Name the blood parasite species.
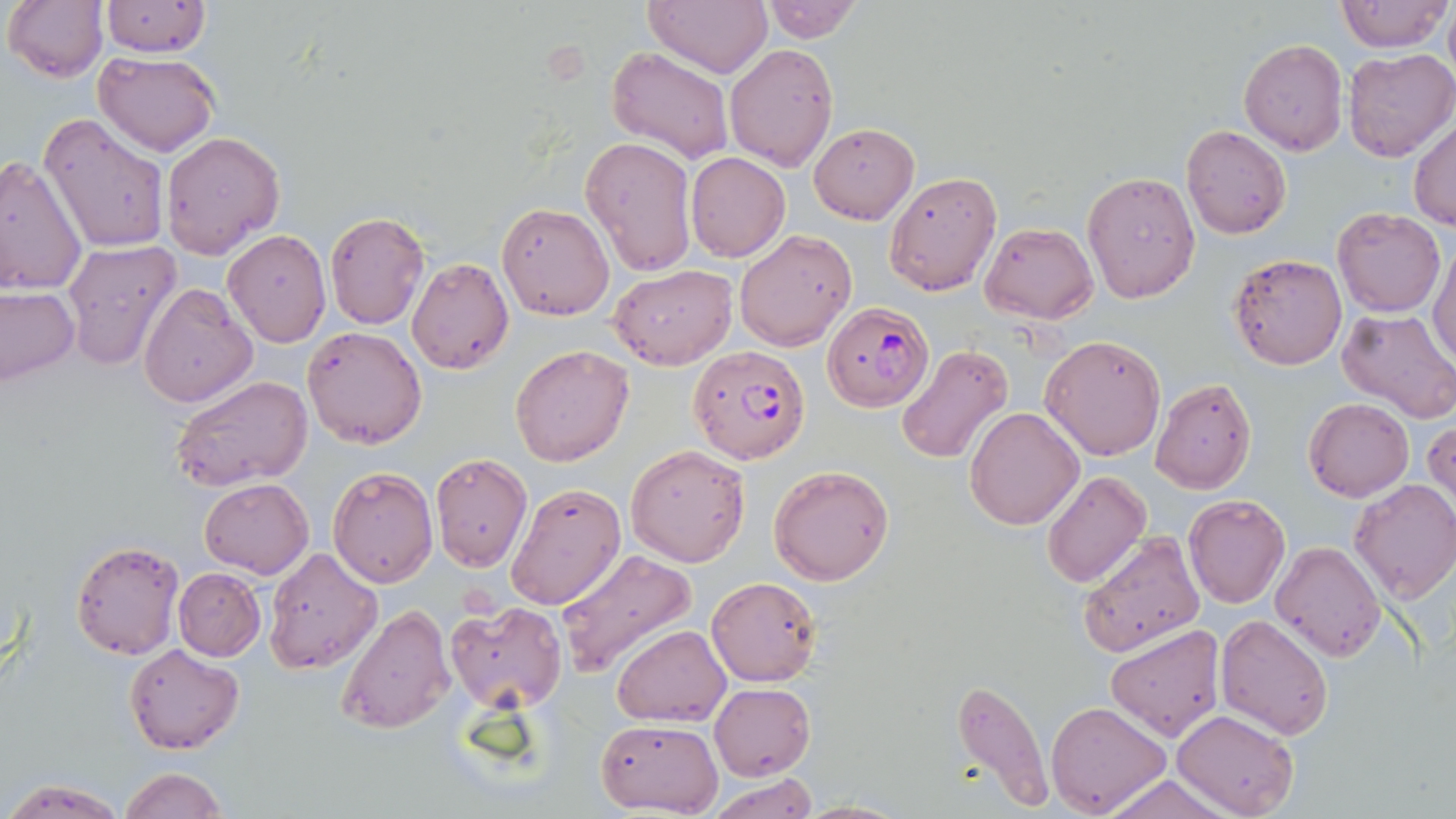

Plasmodium falciparum.

Approximate bounding boxes as (x1, y1, x2, y2) in pixels. Uninfected red blood cell locations: (4, 0, 108, 83), (645, 0, 771, 76), (757, 0, 862, 44), (1336, 0, 1451, 53), (100, 2, 211, 58), (1443, 6, 1455, 80), (1238, 37, 1348, 155), (724, 42, 839, 172), (607, 47, 732, 165), (1342, 47, 1456, 163), (94, 53, 221, 156), (39, 114, 171, 253), (1409, 119, 1455, 230), (809, 123, 918, 224), (1181, 125, 1292, 240), (160, 131, 285, 258), (580, 134, 698, 276), (685, 152, 790, 263), (0, 154, 88, 298), (1082, 170, 1200, 302), (885, 172, 1001, 295), (496, 202, 613, 320), (1333, 208, 1445, 316), (325, 211, 429, 329), (980, 222, 1098, 323), (734, 228, 856, 352), (223, 229, 331, 347), (62, 239, 182, 367), (1429, 240, 1455, 368), (1228, 252, 1346, 371), (406, 256, 514, 374), (611, 265, 736, 370), (138, 282, 257, 407), (0, 285, 80, 386), (1337, 309, 1455, 425), (302, 326, 427, 449), (1040, 334, 1165, 459), (511, 345, 633, 466), (896, 345, 1015, 464), (171, 375, 314, 494), (1150, 377, 1257, 495), (1304, 398, 1414, 502), (965, 408, 1083, 530), (1424, 414, 1455, 518), (625, 443, 751, 568), (428, 452, 532, 572), (769, 463, 895, 586), (328, 466, 439, 588), (1042, 470, 1151, 589), (200, 478, 313, 578), (1349, 478, 1456, 602), (505, 481, 626, 611), (1183, 494, 1290, 609), (1076, 530, 1205, 658), (71, 538, 186, 661), (1269, 540, 1384, 662), (263, 548, 382, 675), (554, 549, 694, 678), (173, 568, 266, 660), (706, 575, 822, 686), (444, 601, 566, 713), (335, 603, 455, 736), (1215, 614, 1334, 738), (1105, 623, 1226, 742), (611, 625, 730, 727), (124, 643, 244, 755), (951, 679, 1053, 810), (708, 683, 815, 780), (1046, 701, 1170, 816), (1173, 709, 1298, 819), (595, 718, 721, 815), (118, 766, 228, 819), (707, 774, 815, 818), (1100, 775, 1231, 819), (5, 777, 124, 817), (793, 797, 908, 817). Plasmodium falciparum-infected red blood cell locations: (821, 303, 935, 413), (688, 344, 812, 463). Light microscopy. Single field of view. Captured at 1000x magnification. May-Grünwald-Giemsa stain. Image is 1456×819 pixels. Thin blood smear.